Comment on the morphology of the erythrocytes.
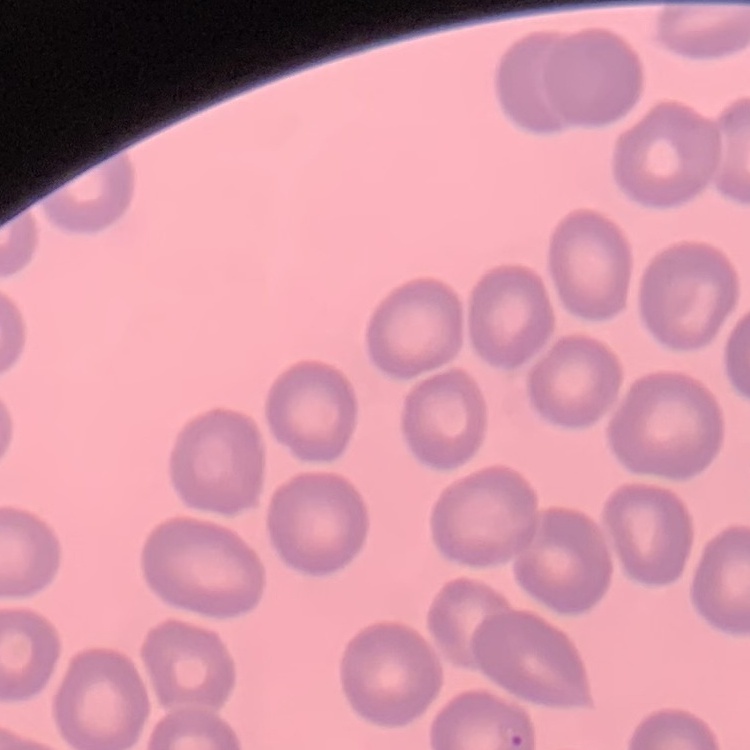

No rouleaux formation.

Square crop of a larger photomicrograph. Thin blood smear. Field's or Giemsa stain.